Locate every Trypanosoma brucei.
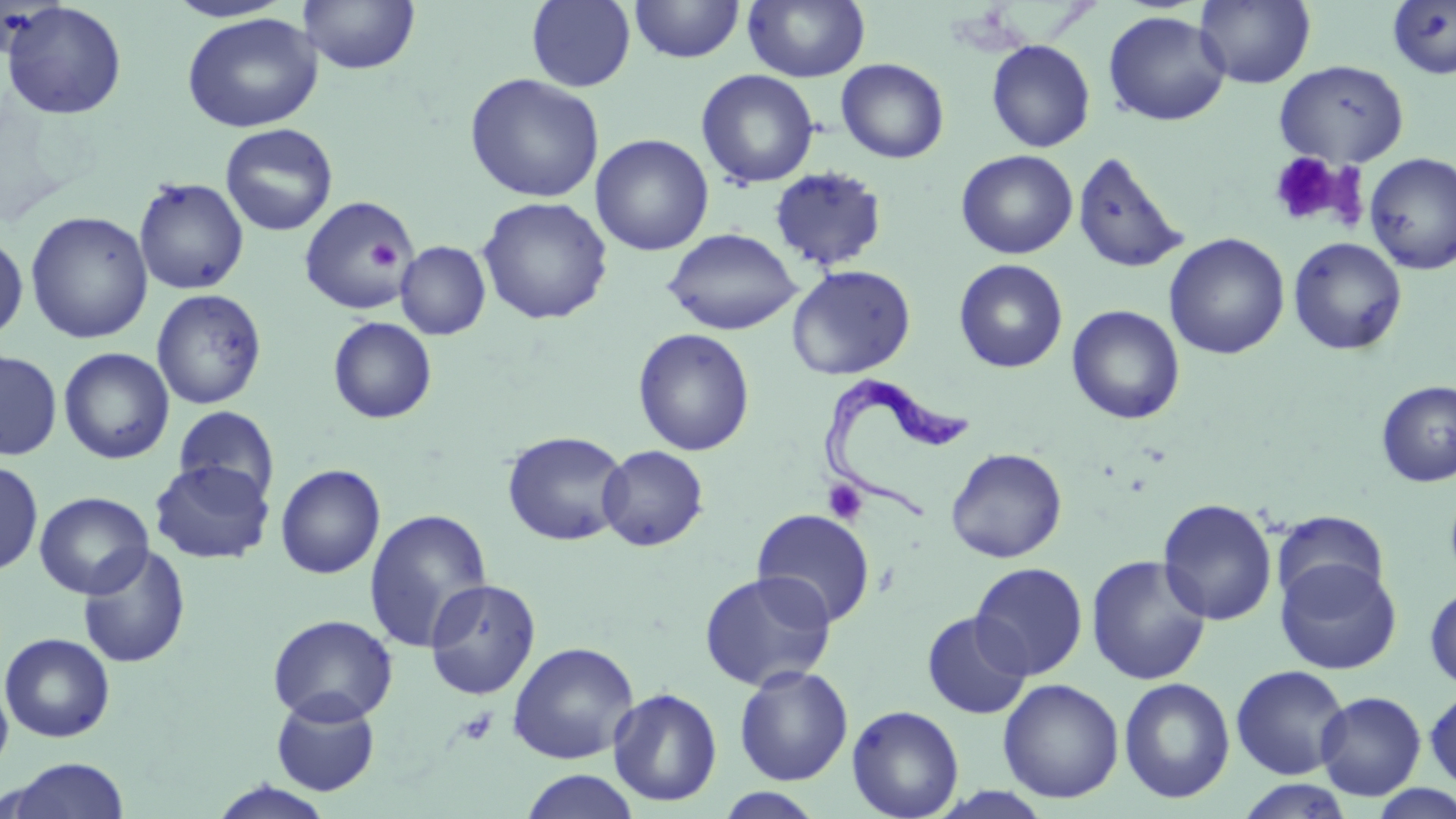
Approximate bounding boxes as [x1, y1, x2, y2] in pixels.
Trypanosoma brucei: [816, 376, 971, 528].

Summary:
  - Platelet locations: [1268, 151, 1346, 226], [367, 238, 401, 273], [823, 479, 868, 526], [455, 707, 498, 747]
  - Uninfected red blood cell locations: [163, 0, 295, 23], [299, 0, 421, 76], [526, 0, 636, 92], [630, 0, 745, 63], [742, 0, 871, 83], [1195, 0, 1316, 89], [2, 1, 128, 120], [1387, 1, 1456, 80], [1102, 11, 1231, 126], [182, 13, 322, 132], [986, 39, 1096, 153], [836, 58, 949, 164], [1274, 60, 1409, 167], [696, 69, 820, 189], [465, 74, 605, 203], [220, 124, 338, 236], [590, 133, 713, 256], [956, 150, 1077, 259], [1072, 151, 1189, 275], [1363, 152, 1456, 274], [769, 166, 886, 273], [133, 177, 249, 295], [298, 195, 416, 315], [477, 196, 613, 325], [25, 211, 153, 344], [664, 228, 802, 335], [0, 233, 28, 343], [1164, 233, 1289, 360], [1287, 236, 1407, 356], [395, 241, 491, 340], [954, 259, 1068, 373], [786, 264, 916, 380], [151, 289, 268, 410], [1066, 305, 1185, 424], [327, 316, 438, 424], [632, 328, 755, 457], [58, 347, 175, 465], [0, 349, 63, 461], [1375, 380, 1456, 487], [174, 406, 280, 503], [502, 430, 630, 547], [597, 445, 709, 551], [945, 447, 1067, 563], [149, 459, 275, 564], [0, 460, 43, 576], [275, 463, 386, 579], [34, 491, 154, 599], [1157, 498, 1277, 625], [364, 508, 493, 654], [751, 508, 875, 627], [1271, 510, 1390, 606], [77, 545, 191, 669], [1085, 555, 1212, 685], [1275, 558, 1402, 675], [970, 562, 1089, 680], [699, 570, 837, 691], [424, 578, 541, 700], [1424, 584, 1456, 690], [922, 611, 1032, 719], [267, 614, 398, 725], [0, 632, 116, 742], [507, 641, 640, 764], [734, 664, 854, 786], [1230, 664, 1350, 779], [1118, 677, 1236, 804], [0, 678, 13, 776], [997, 678, 1125, 804], [608, 687, 723, 808], [1424, 687, 1456, 791], [1315, 691, 1426, 800], [270, 694, 380, 796], [847, 704, 964, 819], [4, 758, 131, 819], [519, 769, 642, 818], [1232, 777, 1358, 819], [208, 781, 337, 819], [1365, 783, 1456, 818], [714, 788, 828, 818]
  - Slide-level diagnosis: Trypanosoma brucei
  - Stain: May-Grünwald-Giemsa
  - Preparation: thin blood smear
  - Field of view: single
  - Modality: optical microscopy
  - Magnification: 1000x
  - Image size: 1456×819 pixels